Give the position of every Plasmodium parasite visible.
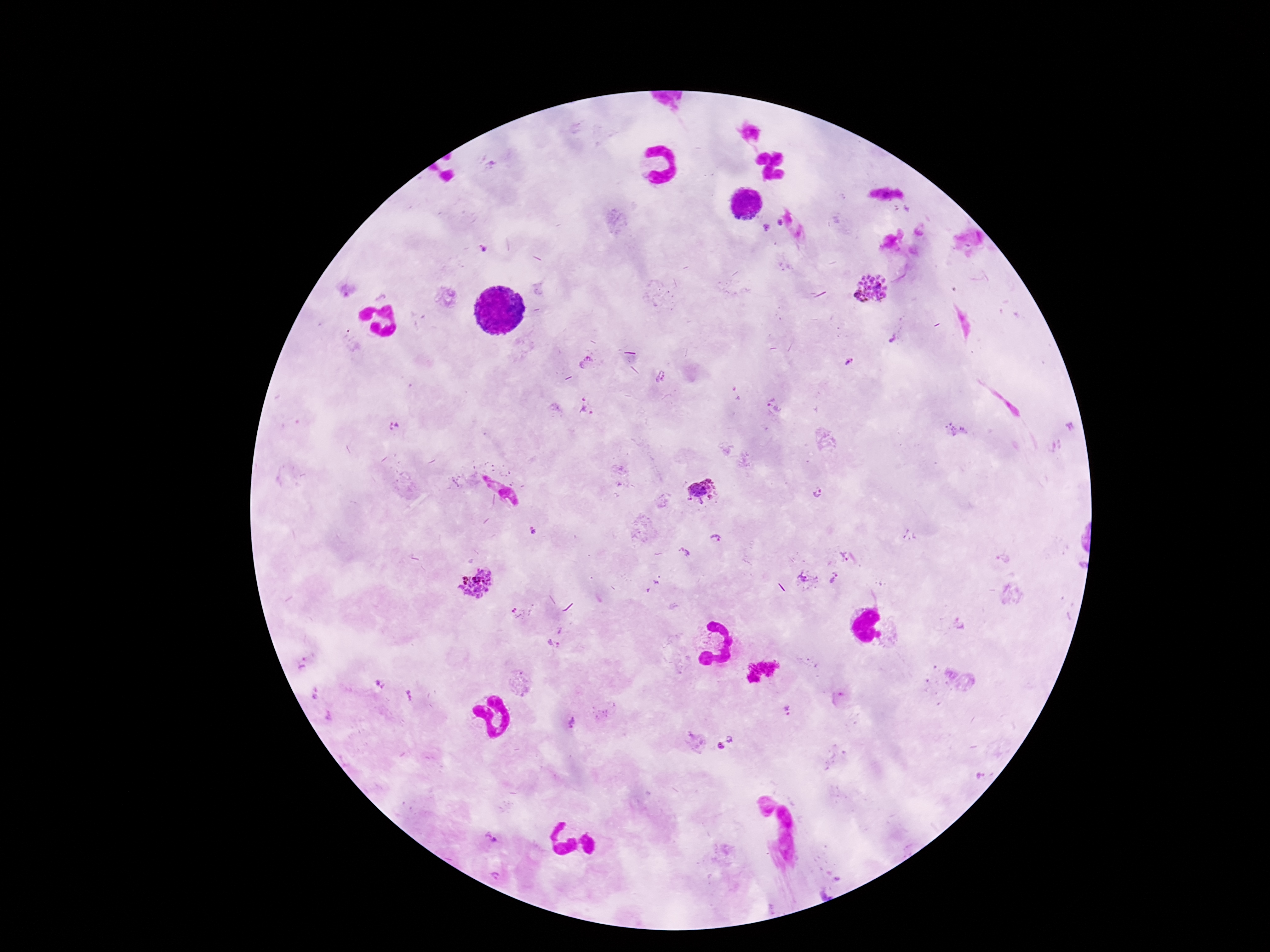
Approximate centers as (x, y) in pixels.
Plasmodium parasites: (779, 222), (767, 227), (484, 249), (871, 288), (346, 292), (892, 340), (849, 361), (586, 364), (660, 377), (774, 406), (587, 407), (395, 426), (956, 431), (703, 491), (819, 494), (532, 532), (716, 538), (685, 552), (850, 558), (1003, 559), (808, 577), (836, 578), (477, 582), (655, 584), (521, 615), (961, 625), (557, 639), (303, 662), (380, 684), (316, 694), (408, 696), (840, 700), (790, 712), (329, 717), (572, 722), (729, 740), (719, 746), (491, 839), (495, 875).

100x magnification. Image is 1270×952 pixels. Thick blood film. Patient malaria status: infected. Giemsa stain. One field from this slide. Photographed through the microscope eyepiece with a smartphone camera.